State which parasite is depicted.
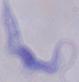

A trypanosome.

1000x magnification. Photomicrograph.